Locate every blood parasite and identify its species.
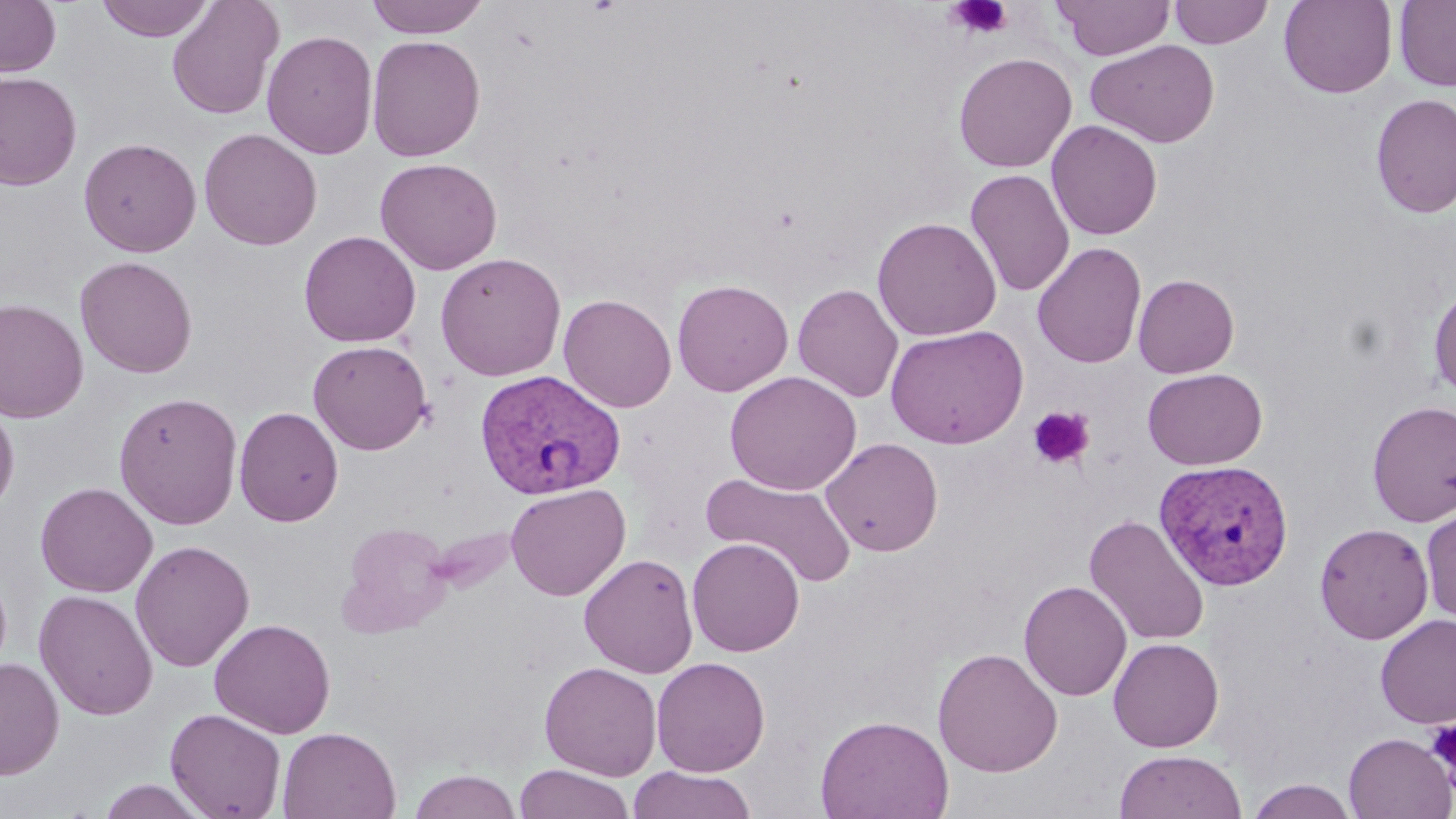

Approximate bounding boxes as named x1/y1/x2/y2 corners in pixels.
Plasmodium vivax-infected red blood cells: (x1=475, y1=369, x2=626, y2=500), (x1=1153, y1=459, x2=1294, y2=590).
No Plasmodium falciparum, Plasmodium ovale, Plasmodium malariae, Babesia divergens, or Trypanosoma brucei observed.

Uninfected red blood cell locations: (x1=0, y1=0, x2=62, y2=77), (x1=97, y1=0, x2=215, y2=42), (x1=166, y1=0, x2=284, y2=120), (x1=364, y1=0, x2=491, y2=38), (x1=1054, y1=0, x2=1174, y2=61), (x1=1168, y1=0, x2=1274, y2=48), (x1=1278, y1=0, x2=1397, y2=98), (x1=1394, y1=0, x2=1456, y2=91), (x1=262, y1=30, x2=378, y2=160), (x1=366, y1=34, x2=486, y2=162), (x1=1086, y1=39, x2=1220, y2=148), (x1=953, y1=52, x2=1077, y2=172), (x1=0, y1=71, x2=82, y2=191), (x1=1370, y1=93, x2=1456, y2=219), (x1=1046, y1=120, x2=1163, y2=240), (x1=198, y1=127, x2=322, y2=251), (x1=78, y1=137, x2=202, y2=257), (x1=374, y1=157, x2=502, y2=275), (x1=965, y1=169, x2=1074, y2=298), (x1=872, y1=217, x2=1001, y2=342), (x1=298, y1=230, x2=421, y2=347), (x1=1032, y1=241, x2=1147, y2=368), (x1=435, y1=253, x2=567, y2=382), (x1=75, y1=255, x2=197, y2=379), (x1=1133, y1=274, x2=1239, y2=378), (x1=671, y1=279, x2=794, y2=397), (x1=792, y1=283, x2=904, y2=402), (x1=1429, y1=285, x2=1456, y2=399), (x1=558, y1=294, x2=677, y2=412), (x1=0, y1=297, x2=89, y2=424), (x1=885, y1=325, x2=1029, y2=449), (x1=307, y1=339, x2=433, y2=455), (x1=1142, y1=368, x2=1267, y2=470), (x1=724, y1=370, x2=862, y2=496), (x1=113, y1=391, x2=244, y2=529), (x1=0, y1=398, x2=19, y2=518), (x1=1367, y1=400, x2=1456, y2=526), (x1=234, y1=406, x2=344, y2=527), (x1=820, y1=438, x2=943, y2=556), (x1=701, y1=471, x2=857, y2=588), (x1=35, y1=481, x2=158, y2=597), (x1=505, y1=484, x2=630, y2=600), (x1=1421, y1=506, x2=1456, y2=626), (x1=1084, y1=515, x2=1210, y2=647), (x1=1314, y1=522, x2=1433, y2=644), (x1=338, y1=524, x2=453, y2=637), (x1=426, y1=524, x2=521, y2=594), (x1=686, y1=538, x2=804, y2=657), (x1=130, y1=540, x2=255, y2=672), (x1=579, y1=553, x2=699, y2=678), (x1=1019, y1=580, x2=1132, y2=701), (x1=34, y1=589, x2=158, y2=720), (x1=1375, y1=614, x2=1456, y2=729), (x1=209, y1=617, x2=336, y2=739), (x1=1108, y1=637, x2=1224, y2=752), (x1=932, y1=648, x2=1063, y2=777), (x1=0, y1=657, x2=64, y2=780), (x1=652, y1=657, x2=771, y2=777), (x1=539, y1=661, x2=662, y2=780), (x1=164, y1=708, x2=287, y2=819), (x1=815, y1=714, x2=954, y2=819), (x1=278, y1=727, x2=401, y2=819), (x1=1343, y1=732, x2=1455, y2=819), (x1=1113, y1=749, x2=1248, y2=819), (x1=514, y1=764, x2=635, y2=819), (x1=628, y1=766, x2=757, y2=818), (x1=407, y1=769, x2=523, y2=818), (x1=96, y1=779, x2=211, y2=818), (x1=1245, y1=779, x2=1360, y2=818). Platelet locations: (x1=947, y1=0, x2=1014, y2=39), (x1=1028, y1=406, x2=1094, y2=469), (x1=1426, y1=719, x2=1456, y2=773). Slide-level diagnosis: Plasmodium vivax. 1000x magnification. Thin blood film. May-Grünwald-Giemsa-stained preparation. Light microscopy. Image is 1456×819 pixels. One field of a larger specimen.